Outline every artifact (stain precipitate or debris).
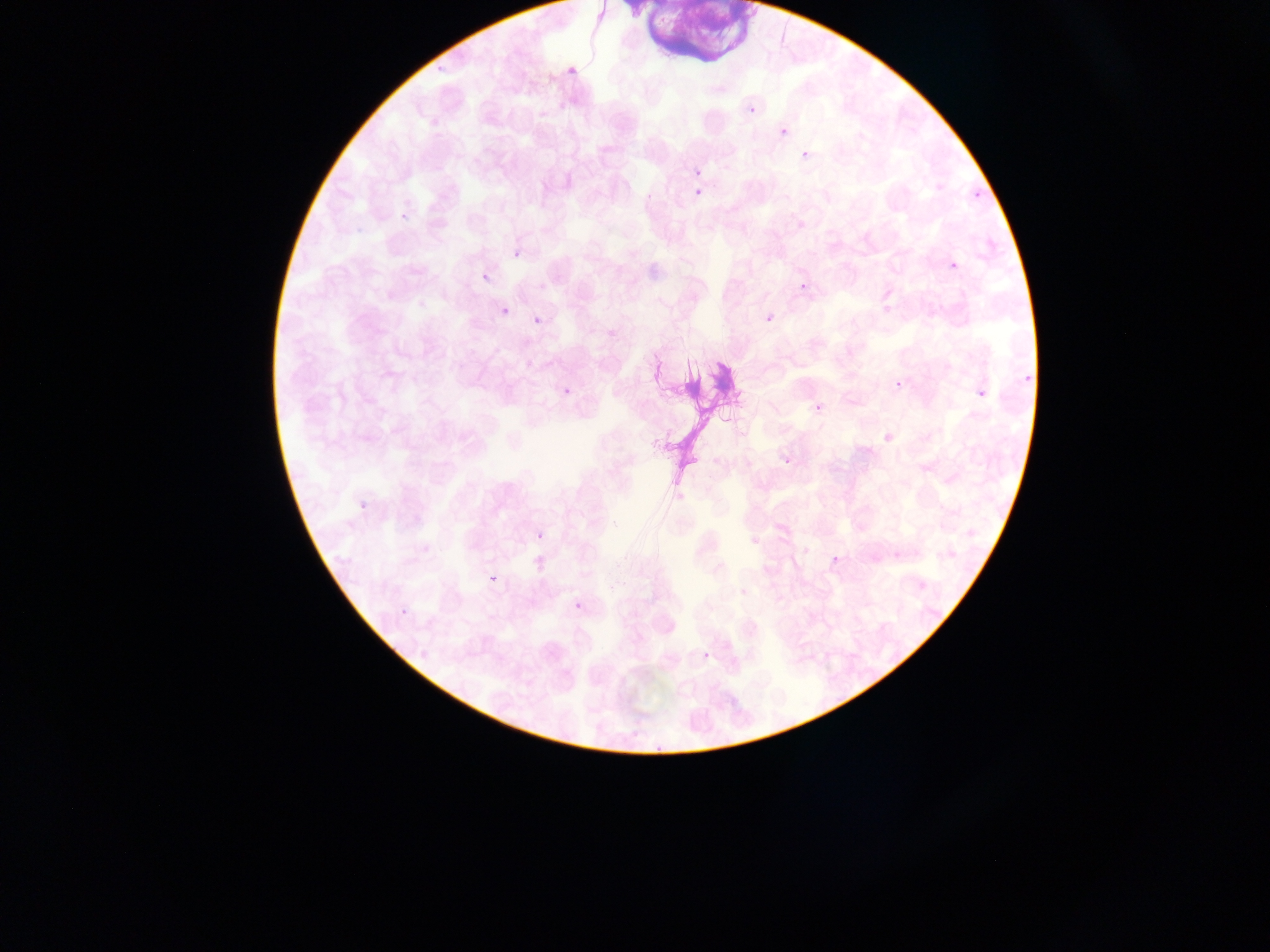

Approximate bounding boxes as left top right bottom in pixels.
Artifacts (stain precipitate or debris): 611 0 746 81; 645 335 734 488.

Summary:
  - Plasmodium parasite locations: 433 60 449 72; 563 67 571 77; 747 103 755 113; 780 128 788 135; 801 151 808 159; 966 172 994 202; 643 184 665 202; 694 189 701 197; 395 210 404 224; 513 250 521 259; 947 253 962 273; 482 272 490 284; 797 277 814 290; 503 307 511 316; 766 314 774 323; 532 316 541 324; 1024 375 1036 384; 555 378 574 396; 897 380 905 389; 972 380 991 404; 812 393 829 413; 781 460 794 473; 354 495 370 513; 535 531 545 541; 892 550 901 559; 832 555 840 563; 485 569 504 587; 397 596 410 616; 574 601 583 610; 702 651 711 660 | approximate x y pixel centers of objects too small to bound: 697 172
  - Image size: 1270×952 pixels
  - Preparation: thin blood film
  - Country: Ghana
  - Capture: mobile-phone photograph through a microscope
  - Field of view: single